Point out each Plasmodium parasite.
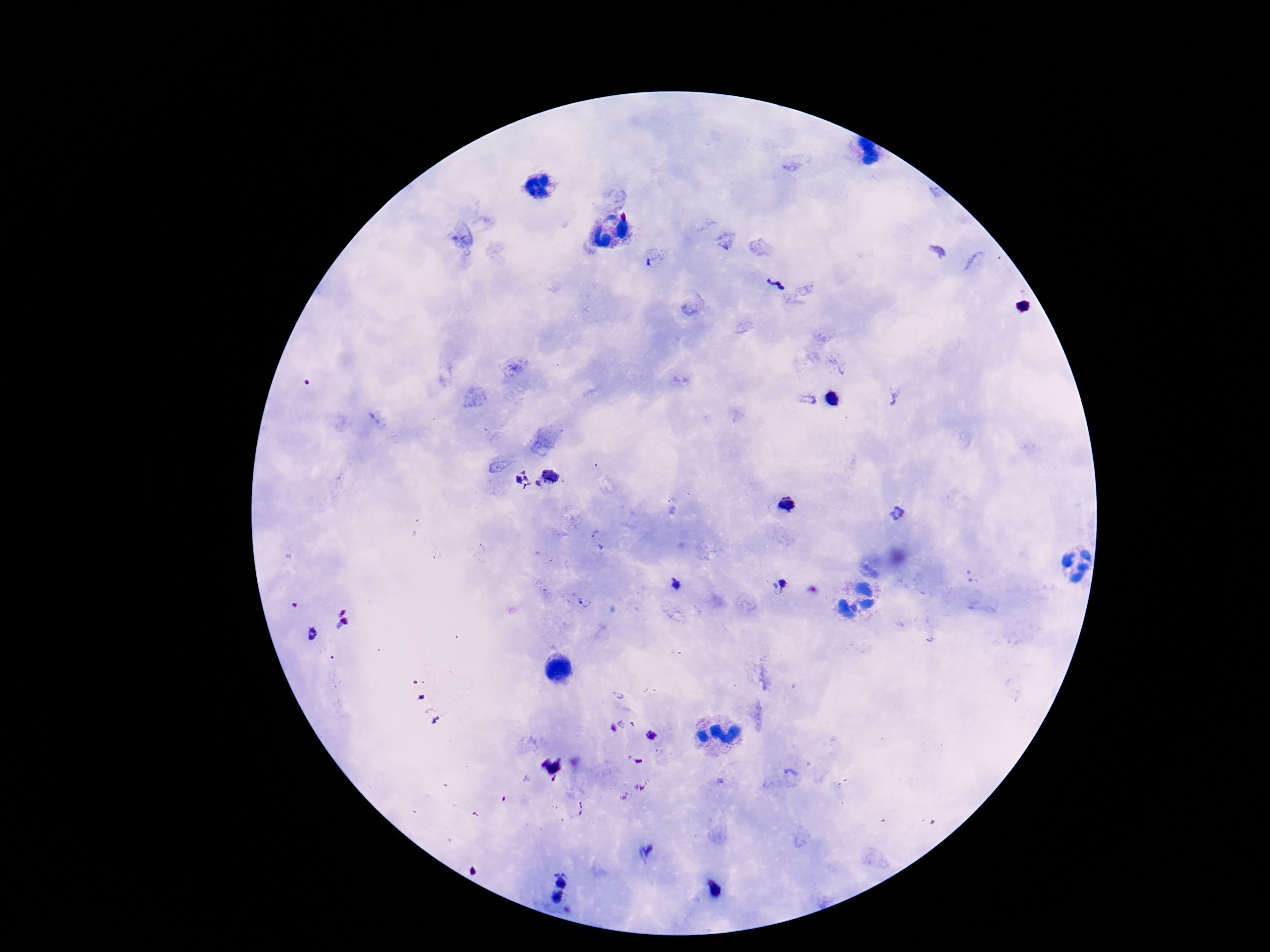
Approximate object centers, in pixels from the top-left corner.
Plasmodium parasites: (x=650, y=263), (x=775, y=283), (x=834, y=400), (x=548, y=478), (x=522, y=480), (x=789, y=504), (x=897, y=514), (x=596, y=534), (x=783, y=584), (x=675, y=586), (x=585, y=602), (x=618, y=695), (x=650, y=735), (x=646, y=851), (x=562, y=878), (x=714, y=889), (x=558, y=897).

Photographed through the microscope eyepiece with a smartphone camera. One field from this slide. Patient malaria status: infected. 100x magnification. Thick blood smear. Giemsa-stained preparation. Image is 1270×952 pixels.